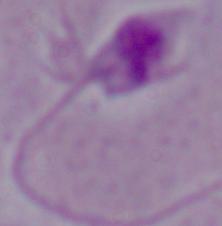

Photomicrograph. A Leishmania parasite is shown. 1000x magnification.